Assess this cell for malaria.
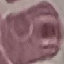

Uninfected.

Photographed with a smartphone camera at the microscope eyepiece. Automatically extracted cell patch, resized to 64 × 64 pixels. Giemsa-stained preparation. Thin smear of blood.